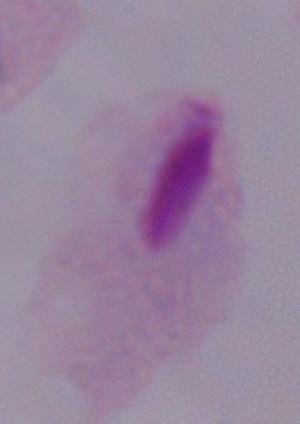

identification: trichomonad
modality: micrograph
magnification: 1000x